Identify the cell.
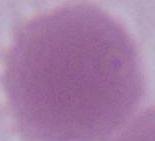

An erythrocyte.

{
  "modality": "photomicrograph",
  "magnification": "1000x"
}